Report the malaria status of this cell.
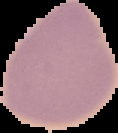

It is uninfected.

preparation = thin blood smear
image type = segmented cell region on a black background
image size = 118×133 pixels